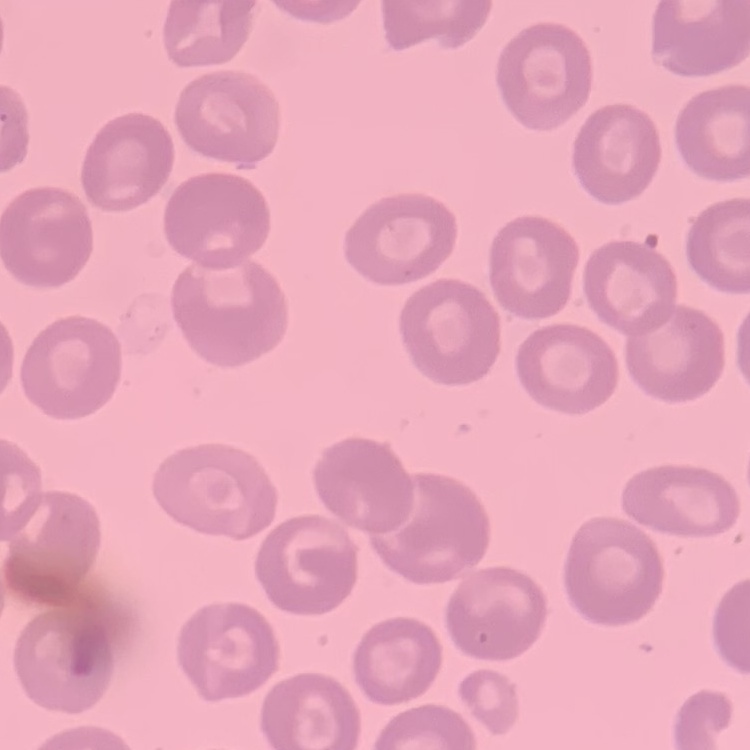

erythrocyte_morphology: no rouleaux formation
image_type: square crop of a larger photomicrograph
stain: Field's or Giemsa
preparation: thin blood film